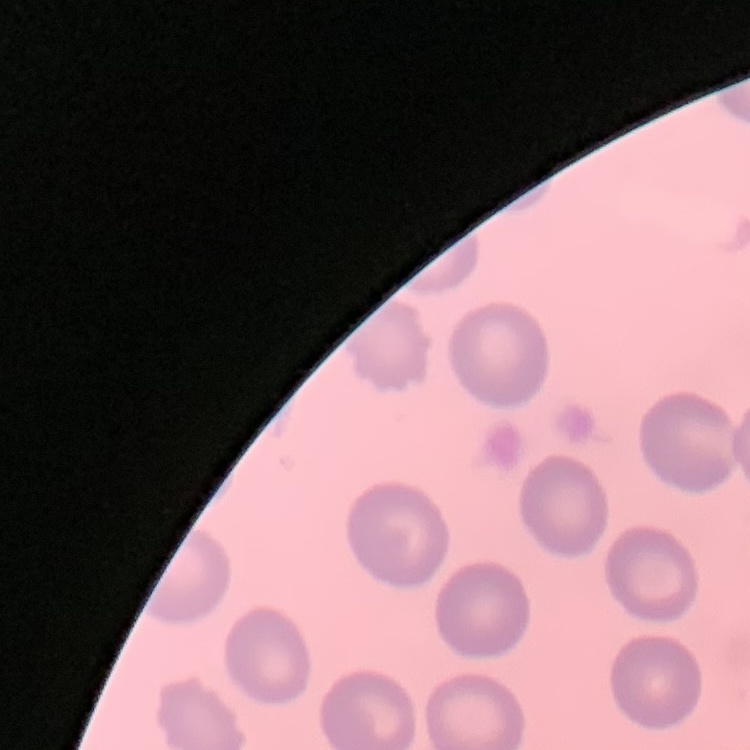
Summary:
  - Red blood cell morphology: no rouleaux formation
  - Preparation: thin peripheral smear
  - Stain: Field's or Giemsa
  - Image type: square crop of a larger photomicrograph